Outline each Plasmodium falciparum-infected red blood cell.
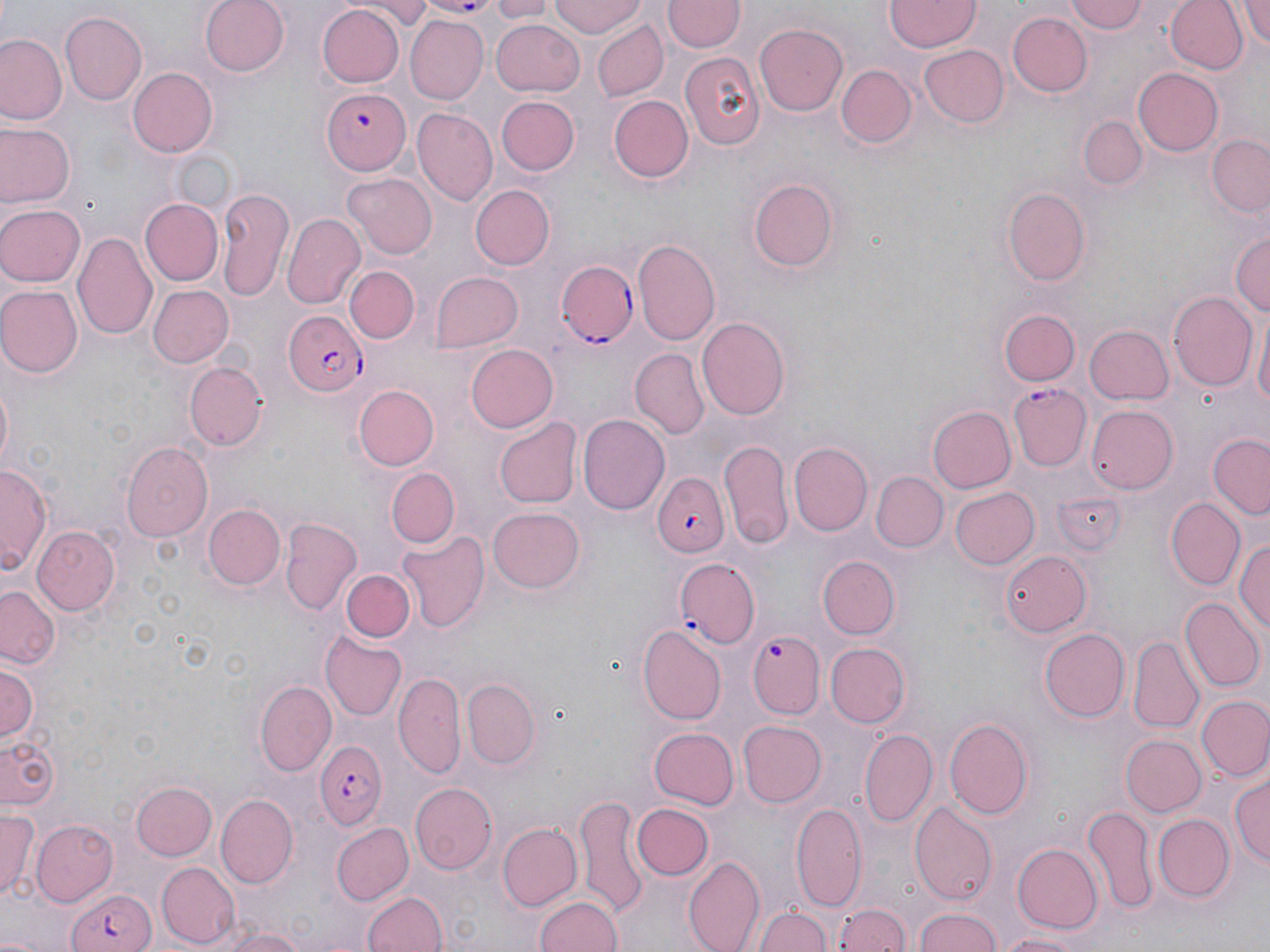

Approximate bounding boxes as [x1, y1, x2, y2] in pixels.
Plasmodium falciparum-infected red blood cells: [430, 0, 499, 17], [325, 87, 410, 174], [557, 261, 639, 345], [281, 311, 369, 397], [1010, 384, 1091, 470], [650, 474, 731, 559], [671, 557, 760, 646], [746, 631, 825, 719], [315, 743, 387, 828], [65, 888, 154, 952].

slide-level diagnosis = Plasmodium falciparum
field of view = one of a larger specimen
magnification = 1000x
stain = May-Grünwald-Giemsa
uninfected red blood cell locations = approximate bounding boxes as [x1, y1, x2, y2] in pixels: [201, 0, 290, 76], [361, 0, 437, 26], [486, 0, 554, 21], [549, 0, 644, 38], [1067, 0, 1149, 34], [1166, 0, 1246, 75], [1236, 0, 1270, 51], [664, 1, 744, 53], [884, 1, 981, 51], [317, 5, 404, 88], [1010, 11, 1092, 96], [59, 12, 146, 105], [406, 16, 488, 102], [489, 19, 584, 95], [592, 20, 668, 102], [756, 23, 849, 115], [1, 33, 65, 124], [919, 44, 1007, 127], [680, 53, 764, 151], [837, 65, 915, 147], [128, 68, 217, 155], [1134, 68, 1221, 155], [495, 96, 578, 176], [610, 96, 693, 181], [411, 108, 496, 204], [1082, 117, 1145, 189], [2, 123, 74, 210], [1207, 137, 1269, 220], [343, 174, 436, 258], [746, 176, 840, 274], [470, 185, 555, 270], [1002, 185, 1093, 284], [215, 188, 293, 303], [139, 199, 223, 286], [0, 202, 86, 287], [283, 214, 365, 309], [1229, 223, 1270, 317], [75, 232, 159, 341], [632, 239, 722, 347], [346, 264, 419, 343], [428, 271, 523, 352], [0, 284, 81, 377], [148, 284, 235, 368], [1169, 292, 1258, 393], [1252, 308, 1270, 418], [998, 309, 1080, 387], [696, 316, 789, 421], [1086, 325, 1174, 404], [465, 342, 559, 433], [631, 348, 706, 436], [185, 360, 266, 451], [0, 372, 15, 478], [352, 384, 439, 469], [1088, 403, 1180, 493], [929, 407, 1015, 492], [579, 413, 671, 515], [494, 418, 580, 509], [1203, 429, 1269, 522], [718, 437, 794, 545], [120, 441, 213, 541], [788, 443, 873, 535], [1, 463, 50, 577], [386, 468, 459, 546], [872, 472, 947, 552], [951, 486, 1039, 569], [1166, 499, 1244, 589], [203, 503, 286, 591], [486, 508, 585, 592], [281, 519, 362, 616], [31, 527, 118, 616], [395, 532, 488, 636], [1234, 538, 1270, 639], [1000, 547, 1092, 636], [820, 556, 900, 639], [342, 568, 415, 642], [1, 585, 62, 670], [1182, 597, 1264, 691], [639, 624, 727, 723], [1040, 627, 1130, 722], [320, 630, 407, 721], [1128, 638, 1204, 734], [824, 642, 907, 727], [0, 661, 40, 744], [394, 670, 465, 777], [462, 677, 540, 767], [255, 681, 335, 775], [1197, 696, 1269, 781], [945, 716, 1035, 820], [739, 720, 827, 806], [648, 727, 738, 809], [859, 727, 937, 825], [1121, 735, 1207, 818], [0, 736, 60, 808], [1231, 771, 1269, 876], [132, 781, 217, 860], [410, 782, 497, 873], [218, 793, 297, 887], [575, 795, 649, 915], [910, 799, 997, 903], [791, 802, 867, 911], [631, 803, 713, 881], [1082, 804, 1158, 914], [0, 808, 38, 905], [1155, 814, 1234, 900], [32, 819, 118, 902], [331, 821, 415, 905], [495, 822, 581, 910], [1011, 843, 1101, 934], [683, 854, 764, 952], [156, 861, 238, 948], [361, 889, 447, 952], [532, 892, 626, 952], [755, 904, 830, 952], [832, 904, 913, 952], [914, 907, 1006, 952], [216, 927, 310, 952], [992, 930, 1091, 952]
preparation = thin blood smear
image size = 1270×952 pixels
modality = light microscopy